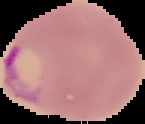

Malaria status: parasitized. Image is 145×124 pixels. From a thin blood smear. The area outside the segmented cell region is set to black.